Describe the morphology of the erythrocytes.
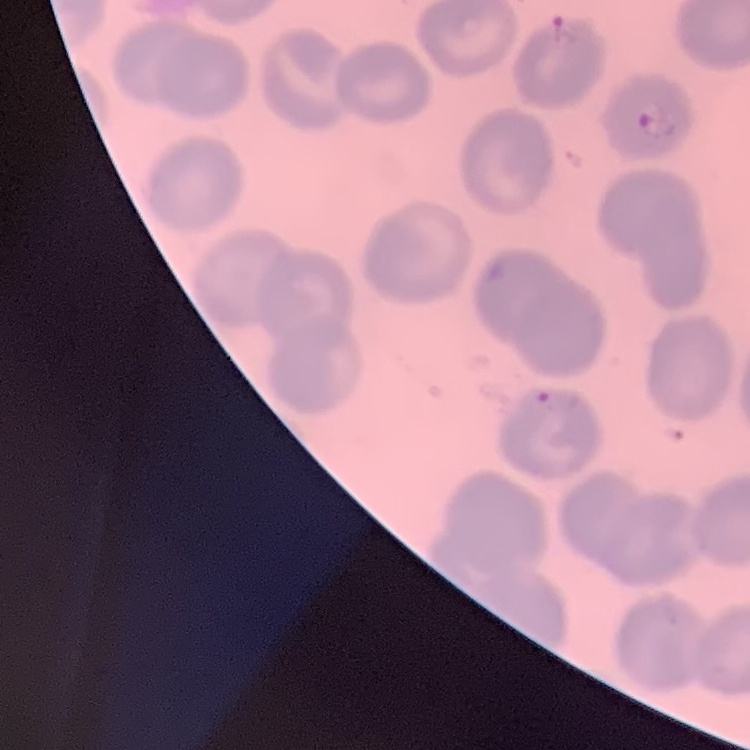
They show no rouleaux formation.

Thin blood smear. Field's or Giemsa stain. Square crop of a larger photomicrograph.